Comment on the morphology of the red blood cells.
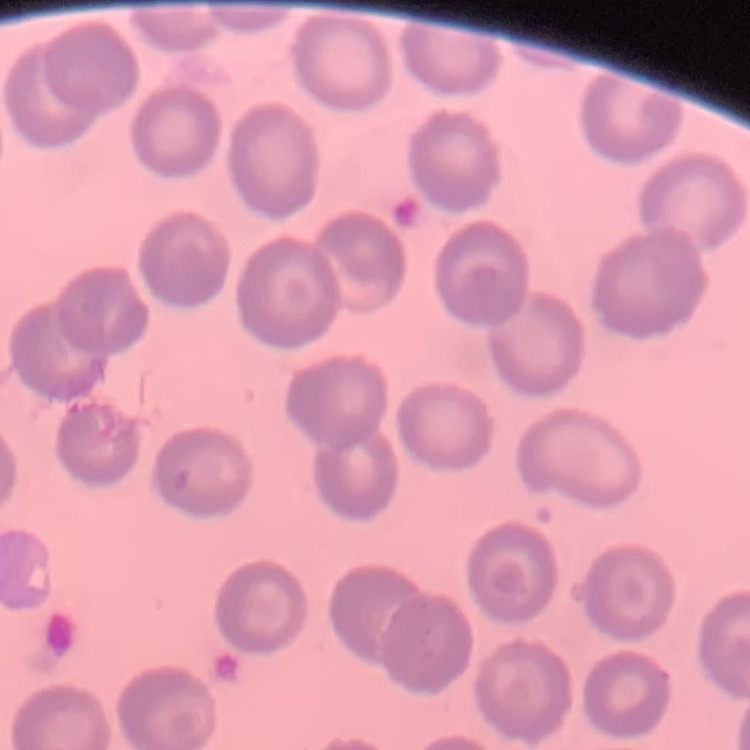
They show no rouleaux formation.

image type = one tile cut from a larger photomicrograph
preparation = thin blood smear
stain = Field's or Giemsa